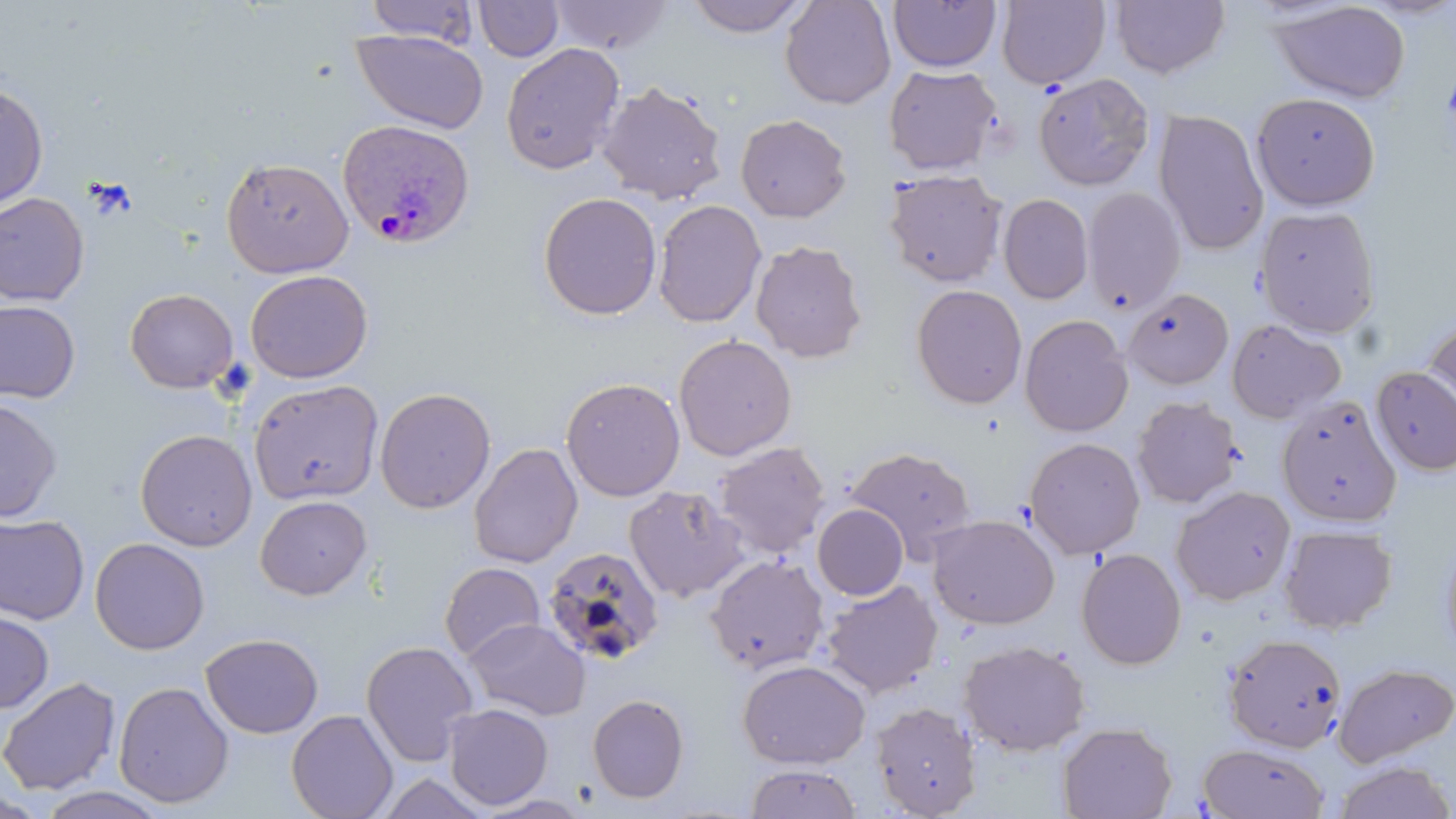

Summary:
  - Coordinate format: approximate bounding boxes as [x1, y1, x2, y2] in pixels
  - Plasmodium ovale-infected red blood cell locations: [336, 118, 476, 250]
  - Uninfected red blood cell locations: [548, 0, 672, 56], [685, 0, 810, 37], [780, 0, 897, 110], [997, 0, 1110, 89], [1110, 0, 1230, 78], [363, 1, 479, 46], [474, 1, 564, 62], [888, 1, 1002, 72], [1270, 2, 1412, 104], [351, 27, 489, 134], [500, 42, 625, 175], [883, 64, 1001, 175], [1033, 72, 1155, 191], [597, 80, 727, 205], [0, 83, 48, 212], [1251, 92, 1381, 212], [1153, 109, 1269, 256], [735, 114, 852, 223], [220, 156, 355, 278], [883, 168, 1009, 287], [1081, 187, 1186, 314], [0, 192, 90, 306], [537, 192, 662, 321], [998, 193, 1094, 304], [653, 199, 766, 328], [1254, 206, 1381, 338], [750, 239, 869, 364], [245, 269, 373, 383], [911, 284, 1028, 410], [124, 288, 238, 393], [1123, 288, 1234, 389], [0, 299, 81, 404], [1422, 314, 1455, 431], [1019, 315, 1133, 437], [1226, 318, 1345, 423], [673, 334, 797, 461], [1371, 366, 1456, 475], [561, 377, 686, 502], [248, 379, 384, 505], [374, 387, 496, 514], [1131, 396, 1244, 508], [0, 397, 62, 523], [1276, 397, 1401, 527], [135, 429, 257, 551], [1024, 437, 1145, 559], [712, 441, 831, 559], [468, 443, 582, 568], [844, 446, 976, 559], [623, 485, 749, 603], [1171, 485, 1296, 605], [255, 495, 372, 600], [813, 504, 909, 600], [0, 513, 90, 625], [927, 514, 1059, 630], [1278, 524, 1398, 634], [1438, 530, 1456, 664], [89, 537, 210, 655], [542, 546, 665, 666], [1076, 548, 1187, 670], [705, 554, 830, 675], [439, 562, 546, 662], [820, 579, 942, 698], [0, 608, 54, 714], [463, 618, 590, 721], [1222, 632, 1347, 753], [200, 633, 324, 739], [360, 640, 479, 766], [958, 640, 1091, 757], [736, 659, 871, 769], [1333, 662, 1454, 766], [0, 676, 121, 796], [113, 680, 235, 809], [587, 694, 690, 804], [870, 701, 981, 817], [443, 703, 553, 810], [286, 709, 398, 819], [1056, 721, 1177, 819], [1198, 743, 1330, 818], [1332, 760, 1455, 819], [744, 764, 863, 818], [32, 786, 172, 819]
  - Slide-level diagnosis: Plasmodium ovale
  - Stain: May-Grünwald-Giemsa
  - Modality: optical microscopy
  - Magnification: 1000x
  - Field of view: one of a larger specimen
  - Image size: 1456×819 pixels
  - Preparation: thin blood film